Assess the morphology of the erythrocytes.
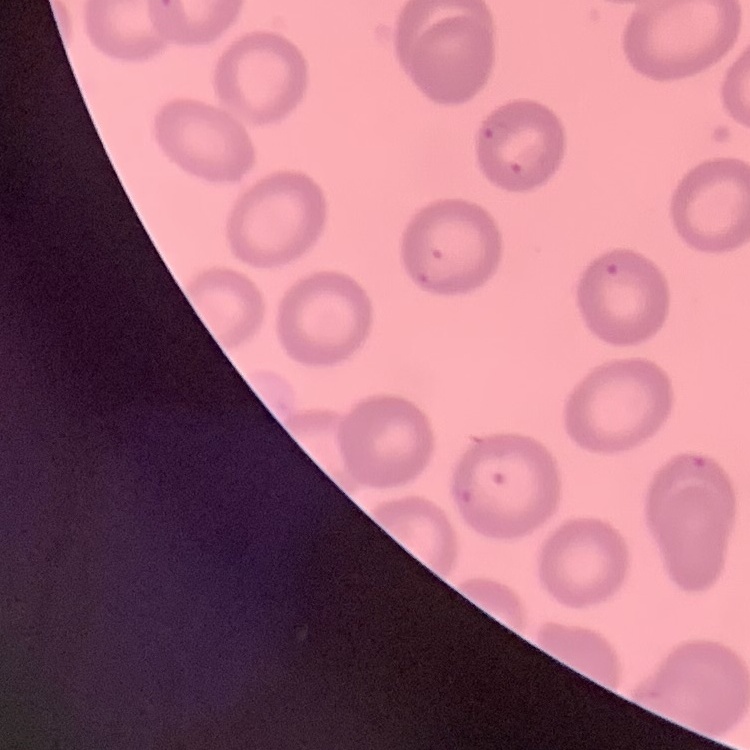

No rouleaux formation.

Field's or Giemsa stain. Thin peripheral smear. One tile cut from a larger photomicrograph.